Identify the blood parasite species.
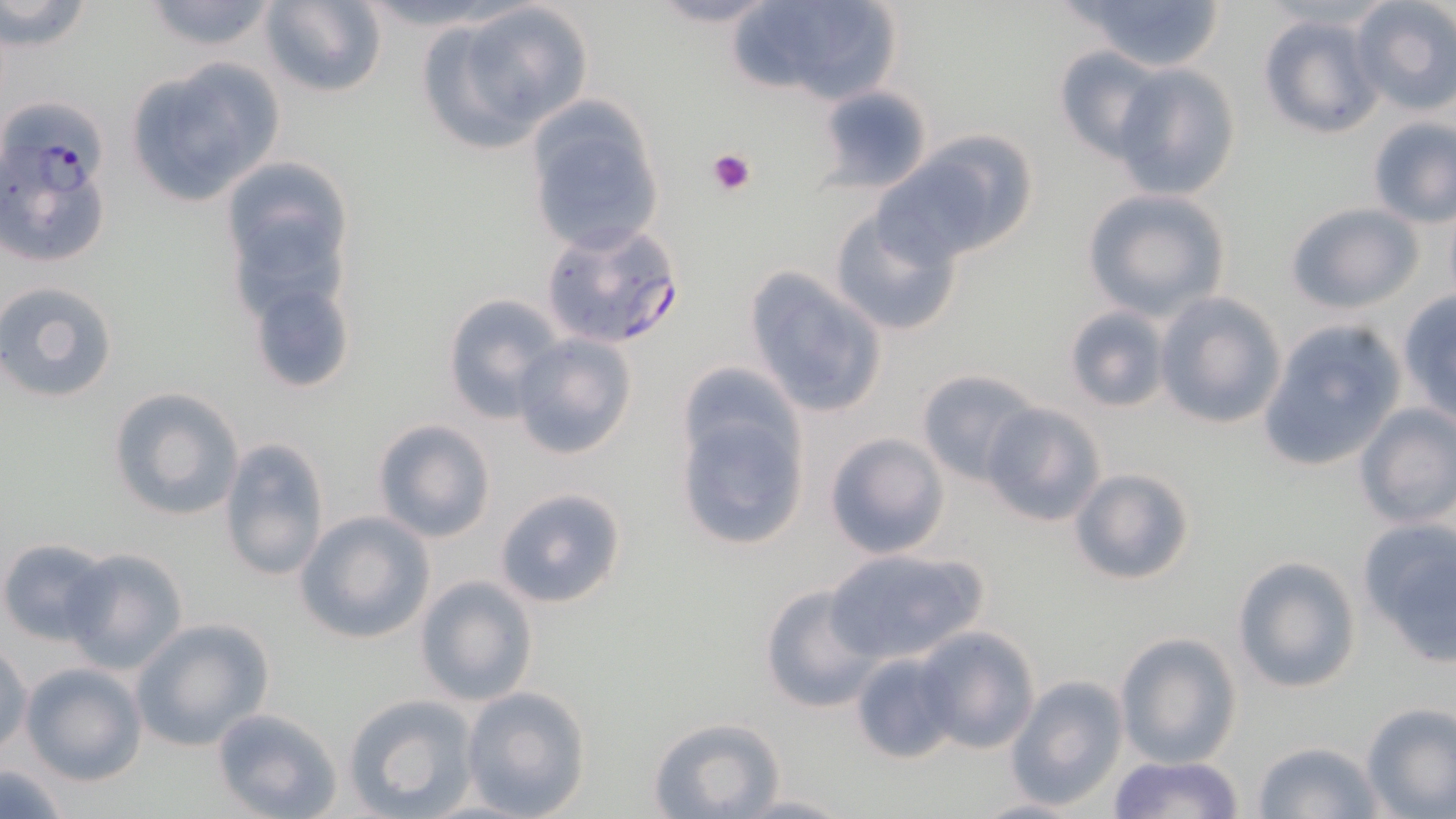

Plasmodium falciparum.

Summary:
  - Coordinate format: approximate bounding boxes as (x1,y1)-(x2,y2) corner pairs in pixels
  - Platelet locations: (707,146)-(757,196)
  - Uninfected red blood cell locations: (136,0)-(286,54), (348,0)-(527,35), (639,0)-(786,29), (728,0)-(901,108), (1065,0)-(1228,72), (1349,0)-(1456,116), (1,1)-(96,52), (258,1)-(387,98), (420,1)-(594,153), (1256,12)-(1385,140), (1053,45)-(1167,162), (123,56)-(286,205), (1113,62)-(1241,201), (816,85)-(936,193), (524,102)-(666,257), (1365,116)-(1455,228), (886,133)-(1037,263), (1081,189)-(1230,321), (1285,201)-(1425,313), (829,204)-(966,338), (241,248)-(360,398), (743,266)-(889,418), (0,279)-(120,404), (1154,291)-(1286,430), (1396,291)-(1456,423), (441,293)-(563,422), (1062,305)-(1171,413), (1258,319)-(1407,471), (510,334)-(638,460), (915,367)-(1041,486), (107,387)-(244,520), (673,400)-(810,552), (979,402)-(1105,528), (1353,403)-(1456,530), (371,418)-(497,542), (823,432)-(951,560), (219,436)-(331,583), (1068,465)-(1196,587), (494,487)-(629,609), (296,511)-(436,644), (1356,518)-(1456,662), (1,537)-(114,645), (64,547)-(189,675), (823,547)-(989,665), (1232,555)-(1362,694), (414,575)-(539,706), (760,584)-(882,713), (132,618)-(273,750), (911,626)-(1041,755), (1114,632)-(1242,769), (0,641)-(32,758), (848,649)-(959,765), (19,662)-(147,785), (1007,675)-(1128,810), (460,686)-(591,817), (343,693)-(478,817), (1359,703)-(1456,818), (211,707)-(344,819), (647,716)-(785,819), (1251,741)-(1387,819), (1107,754)-(1248,818), (0,763)-(72,815), (732,792)-(851,817), (967,796)-(1093,818)
  - Plasmodium falciparum-infected red blood cell locations: (4,106)-(115,271), (541,223)-(684,350)
  - Modality: light microscopy
  - Stain: May-Grünwald-Giemsa
  - Magnification: 1000x
  - Image size: 1456×819 pixels
  - Preparation: thin blood smear
  - Field of view: one of a larger specimen